Name the cell type shown.
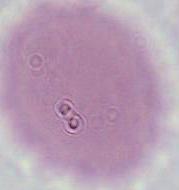

An erythrocyte.

Photomicrograph. Captured at 1000x magnification.